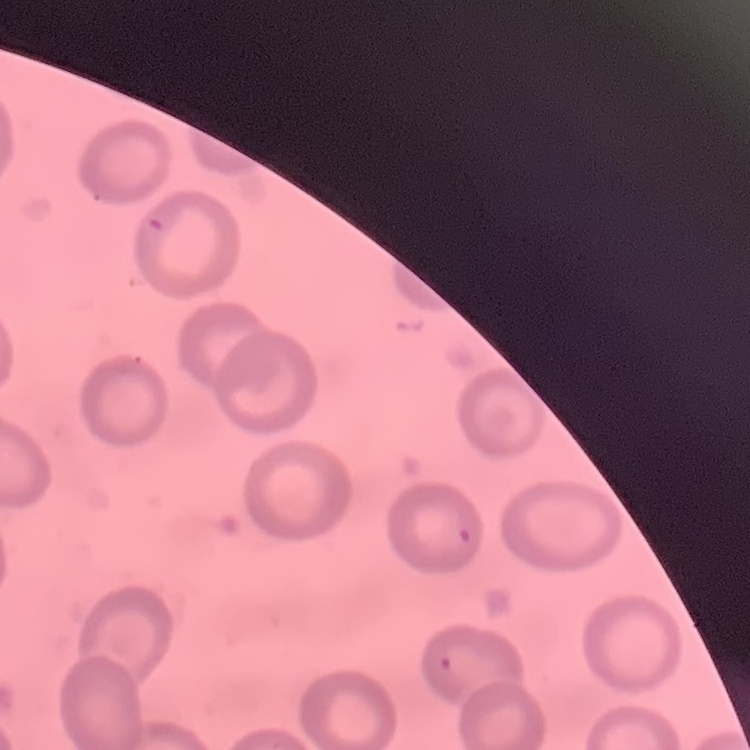

Summary:
  - Red blood cell morphology: no rouleaux formation
  - Stain: Field's or Giemsa
  - Preparation: thin blood smear
  - Image type: square crop of a larger photomicrograph